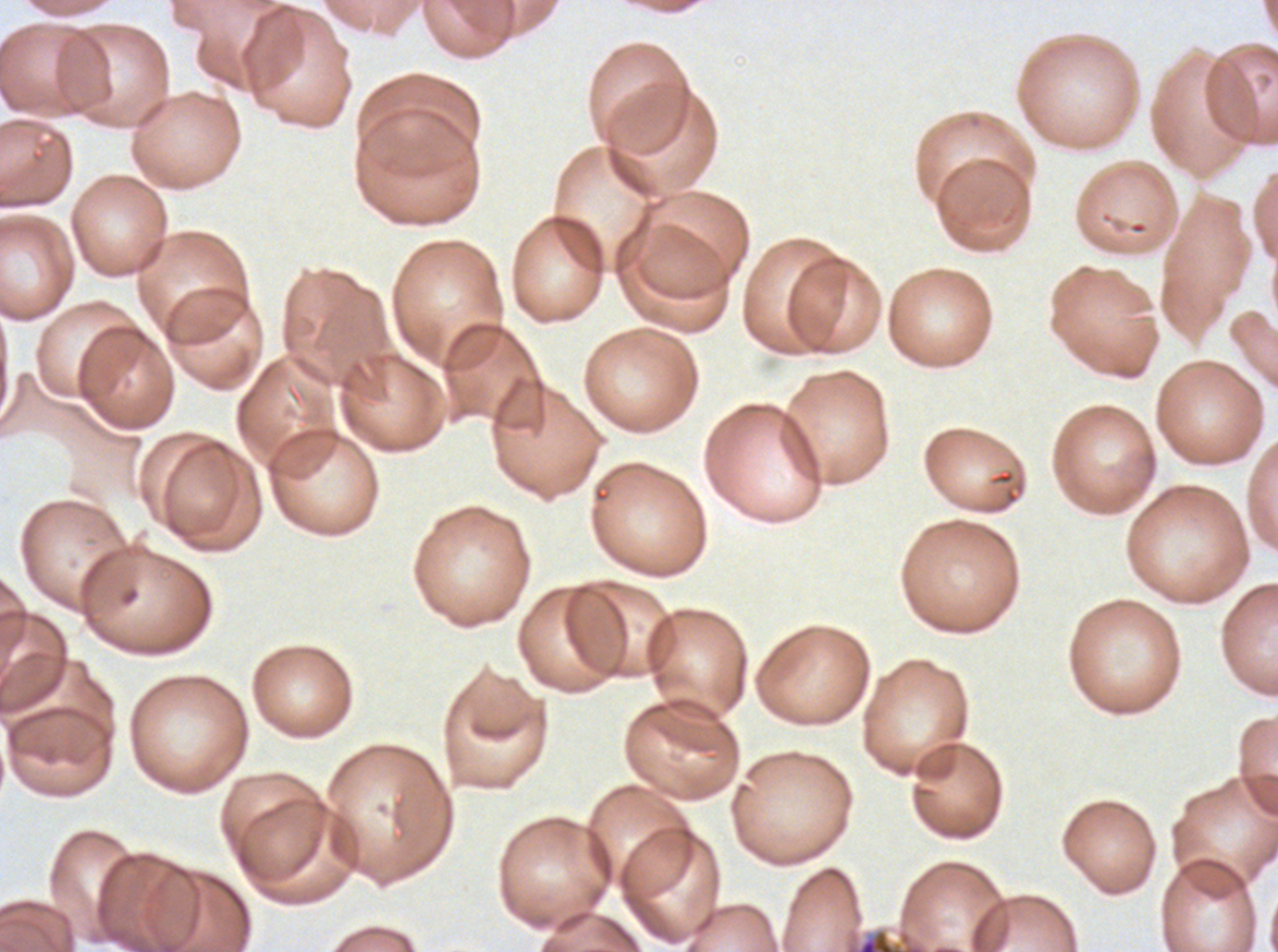 Approximate bounding boxes as {x1, y1, x2, y2} in pixels. Late schizont locations: {844, 927, 927, 951}. Plasmodium falciparum from a patient in The Gambia, cultured ex vivo for 24 to 48 hours. One sub-image of a larger composite. Image is 1278×952 pixels. Giemsa-stained preparation. Thin blood film.